Classify this cell by malaria status.
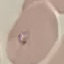

Parasitized.

Thin blood film. Automatically extracted cell patch, resized to 64 × 64 pixels. Photographed with a smartphone camera at the microscope eyepiece. Giemsa stain.